State which parasite is depicted.
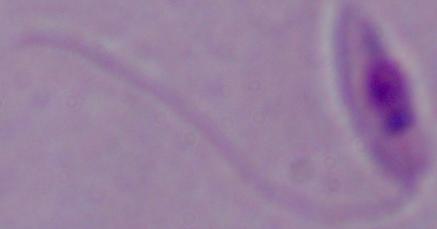

Leishmania.

modality = micrograph
magnification = 1000x